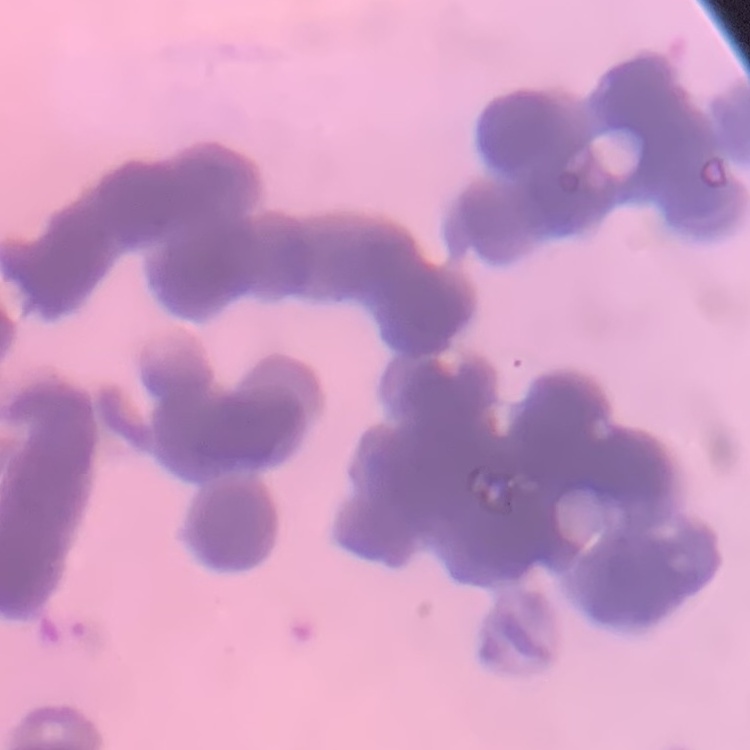

Summary:
  - Erythrocyte morphology: rouleaux formation
  - Stain: Field's or Giemsa
  - Image type: square crop of a larger photomicrograph
  - Preparation: thin blood film